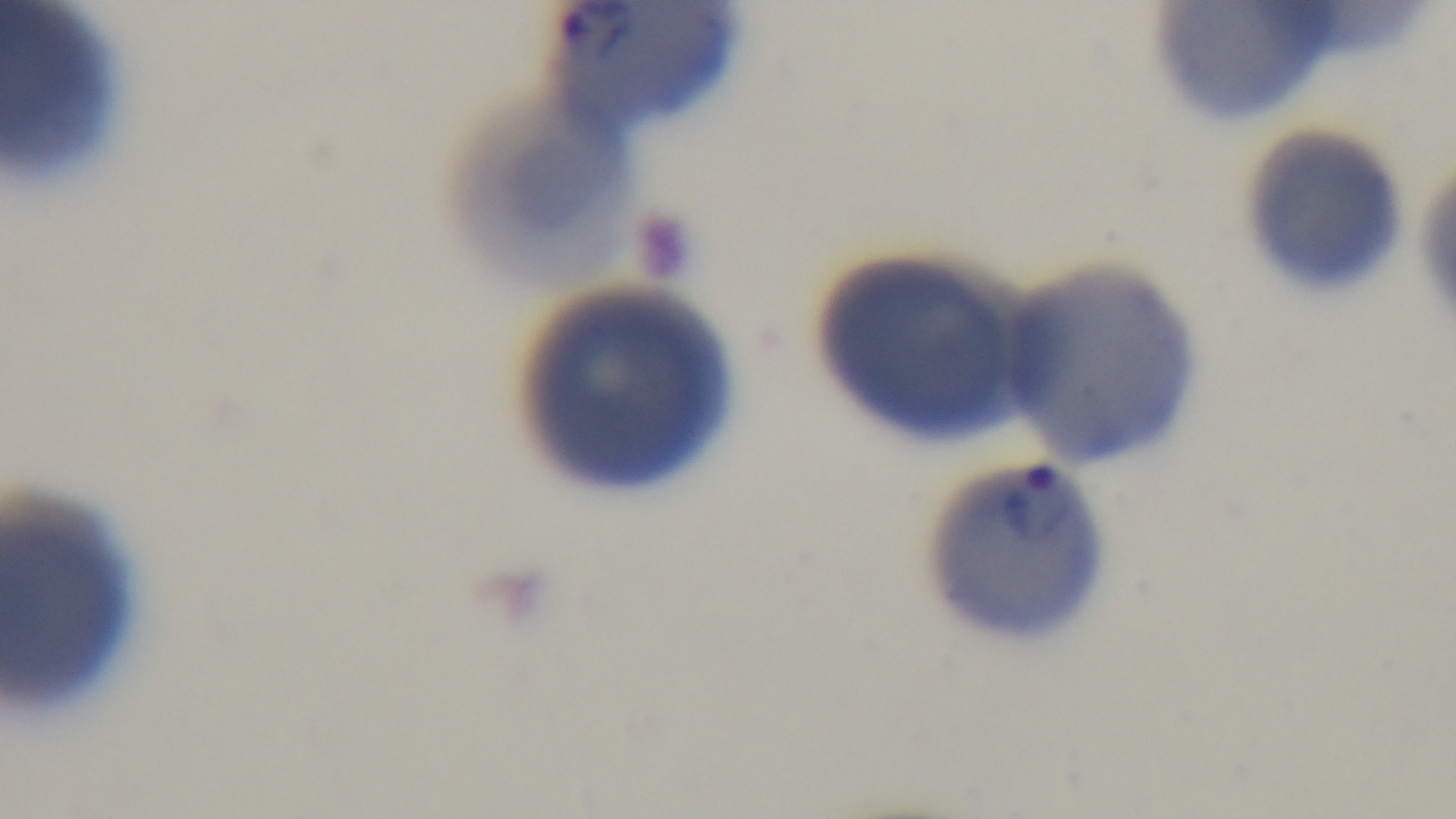
Mounted 4K digital camera. Malaria status: positive. Giemsa-stained. Preparation: thin. Photomicrograph. One field from the slide. 100x oil-immersion objective.